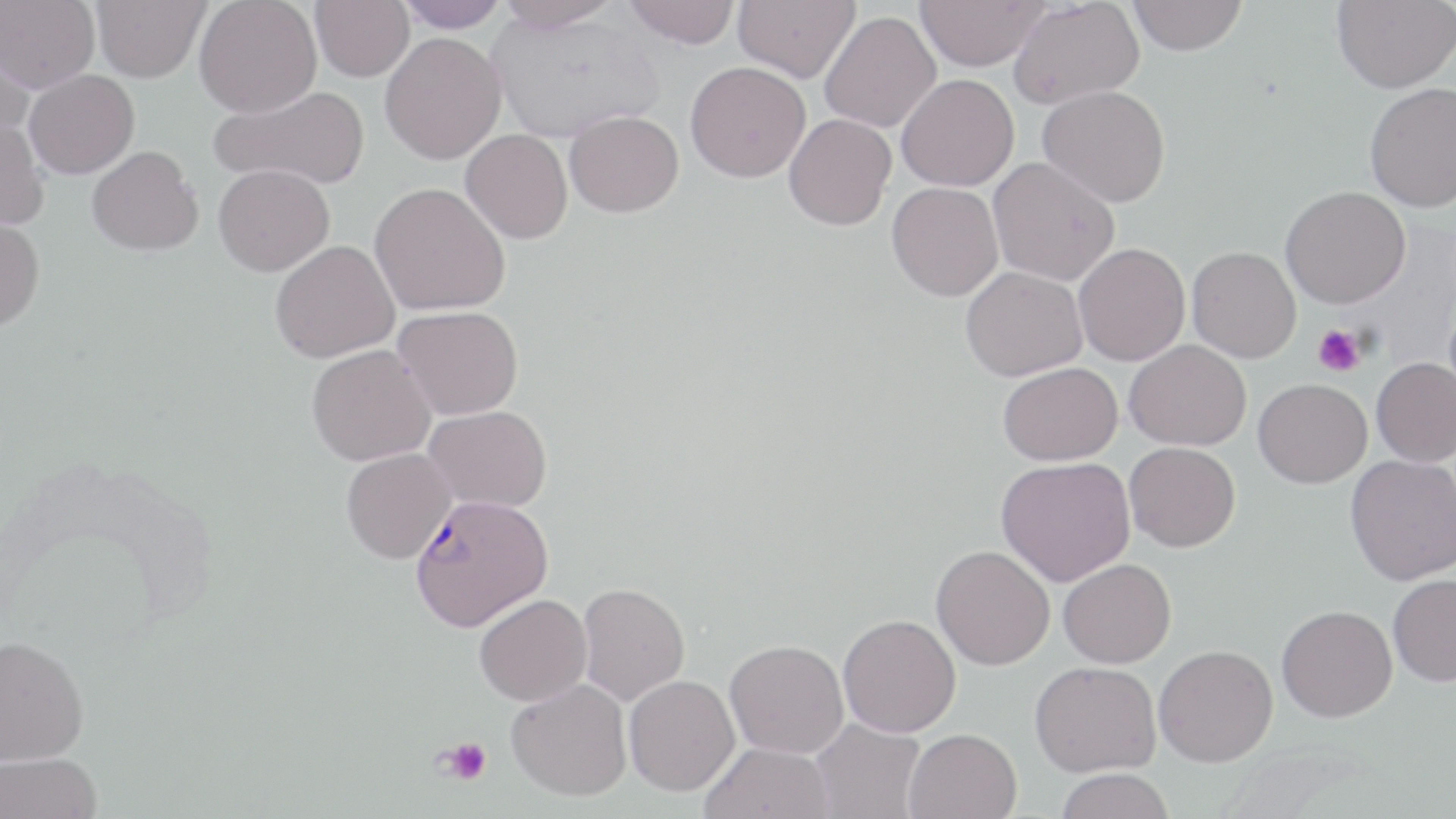

Approximate bounding boxes as named x1/y1/x2/y2 corners in pixels. Uninfected red blood cell locations: (x1=1, y1=0, x2=100, y2=93), (x1=90, y1=0, x2=210, y2=82), (x1=193, y1=0, x2=322, y2=118), (x1=310, y1=0, x2=414, y2=81), (x1=393, y1=0, x2=510, y2=32), (x1=494, y1=0, x2=624, y2=32), (x1=624, y1=0, x2=740, y2=49), (x1=733, y1=0, x2=860, y2=82), (x1=915, y1=0, x2=1049, y2=71), (x1=1008, y1=0, x2=1145, y2=111), (x1=1129, y1=0, x2=1248, y2=56), (x1=1332, y1=0, x2=1456, y2=93), (x1=487, y1=9, x2=663, y2=144), (x1=819, y1=11, x2=941, y2=133), (x1=0, y1=32, x2=37, y2=138), (x1=379, y1=32, x2=506, y2=164), (x1=685, y1=61, x2=811, y2=182), (x1=24, y1=70, x2=140, y2=178), (x1=896, y1=73, x2=1019, y2=191), (x1=1364, y1=82, x2=1456, y2=213), (x1=210, y1=84, x2=370, y2=190), (x1=1037, y1=85, x2=1171, y2=207), (x1=565, y1=110, x2=684, y2=217), (x1=783, y1=113, x2=896, y2=231), (x1=0, y1=114, x2=50, y2=231), (x1=460, y1=129, x2=573, y2=244), (x1=87, y1=146, x2=203, y2=256), (x1=988, y1=156, x2=1120, y2=286), (x1=213, y1=163, x2=334, y2=276), (x1=887, y1=181, x2=1004, y2=301), (x1=369, y1=182, x2=510, y2=316), (x1=1280, y1=185, x2=1410, y2=309), (x1=0, y1=213, x2=45, y2=330), (x1=270, y1=240, x2=399, y2=363), (x1=1074, y1=243, x2=1190, y2=366), (x1=1186, y1=246, x2=1301, y2=363), (x1=960, y1=265, x2=1089, y2=382), (x1=394, y1=305, x2=524, y2=420), (x1=1125, y1=340, x2=1251, y2=451), (x1=306, y1=344, x2=436, y2=466), (x1=1371, y1=357, x2=1456, y2=467), (x1=997, y1=362, x2=1124, y2=465), (x1=1253, y1=378, x2=1372, y2=488), (x1=424, y1=405, x2=552, y2=512), (x1=1124, y1=442, x2=1240, y2=552), (x1=341, y1=447, x2=457, y2=564), (x1=1345, y1=454, x2=1456, y2=585), (x1=996, y1=456, x2=1136, y2=587), (x1=931, y1=544, x2=1055, y2=670), (x1=1058, y1=559, x2=1176, y2=668), (x1=1388, y1=574, x2=1456, y2=687), (x1=577, y1=582, x2=690, y2=706), (x1=474, y1=594, x2=592, y2=706), (x1=1276, y1=605, x2=1397, y2=722), (x1=838, y1=614, x2=961, y2=737), (x1=0, y1=635, x2=89, y2=765), (x1=725, y1=639, x2=849, y2=758), (x1=1154, y1=644, x2=1277, y2=767), (x1=1030, y1=661, x2=1161, y2=777), (x1=624, y1=675, x2=740, y2=796), (x1=507, y1=678, x2=632, y2=801), (x1=810, y1=718, x2=925, y2=819), (x1=904, y1=728, x2=1021, y2=819), (x1=699, y1=741, x2=835, y2=819), (x1=0, y1=752, x2=103, y2=819), (x1=1055, y1=768, x2=1174, y2=819). Platelet locations: (x1=1314, y1=324, x2=1366, y2=376), (x1=438, y1=737, x2=492, y2=786). Plasmodium falciparum-infected red blood cell locations: (x1=409, y1=493, x2=552, y2=631). Slide-level diagnosis: Plasmodium falciparum. One field of a larger specimen. Light microscopy. Captured at 1000x magnification. Thin blood film. Image is 1456×819 pixels. May-Grünwald-Giemsa stain.